Classify this cell by malaria status.
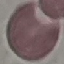

It is uninfected.

Summary:
  - Image type: cell patch, automatically extracted from a larger field of view and resized to 64 × 64 pixels
  - Capture: smartphone through the microscope eyepiece
  - Preparation: thin smear
  - Stain: Giemsa